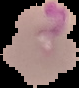

malaria_status: parasitized
image_type: segmented cell region on a black background
image_size: 79×88 pixels
preparation: thin blood smear